Report the malaria status of this cell.
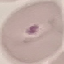
It is parasitized.

{
  "image_type": "cell patch, automatically extracted from a larger field of view and resized to 64 × 64 pixels",
  "stain": "Giemsa",
  "capture": "smartphone through the microscope eyepiece",
  "preparation": "thin blood smear"
}